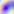

modality = photomicrograph
identification = Toxoplasma gondii
magnification = 400x